Point out each Plasmodium parasite.
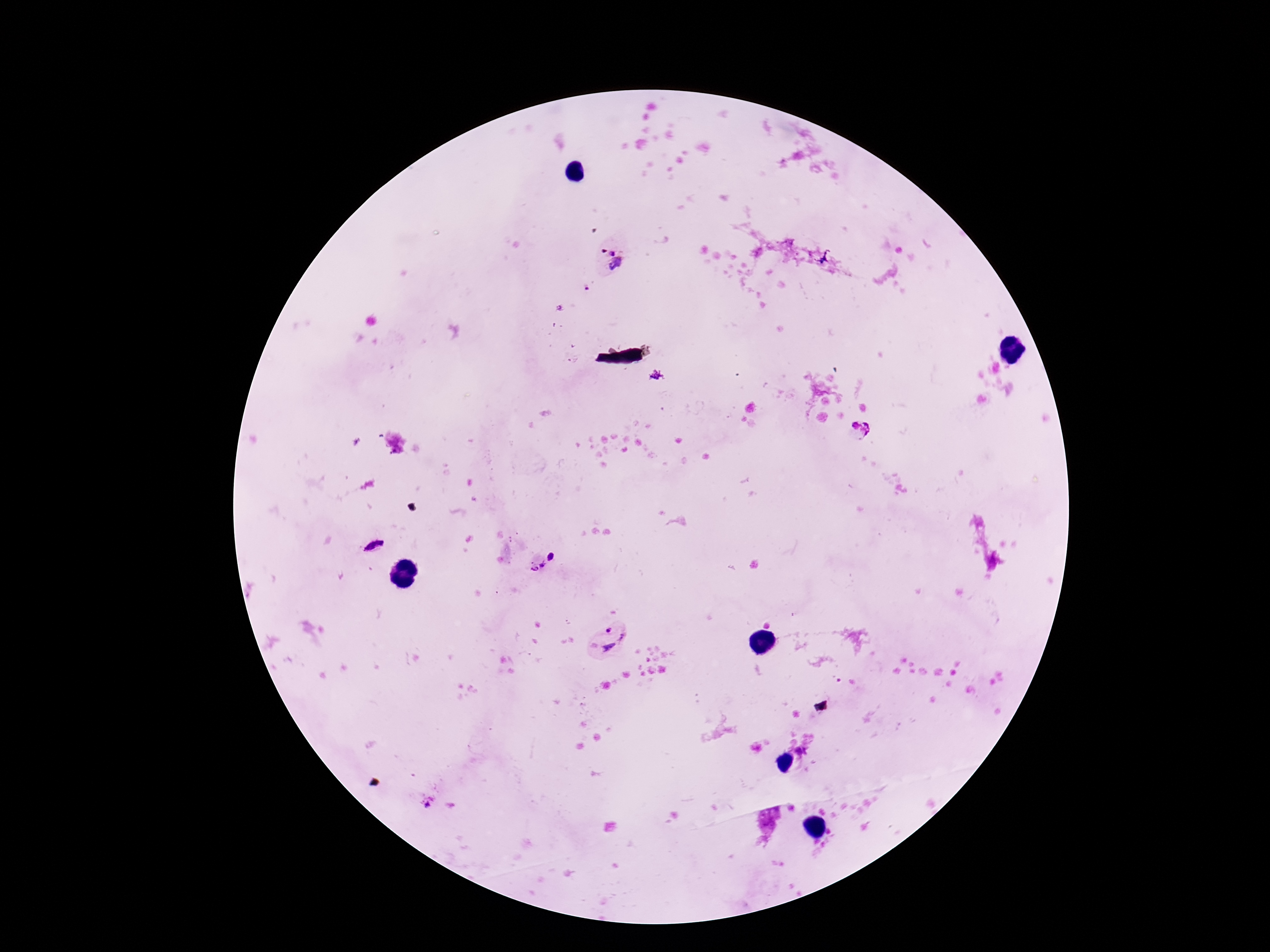

Approximate centers as (x, y) in pixels.
Plasmodium parasites: (610, 258), (372, 544), (551, 555), (533, 563), (619, 640), (428, 802).

Single field of view. Giemsa stain. Photographed through the microscope eyepiece with a smartphone camera. Patient malaria status: positive. Thick blood film. Image is 1270×952 pixels. 100x magnification.